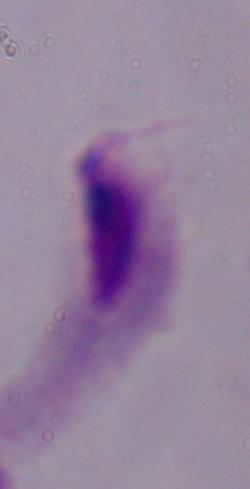
Summary:
  - Magnification: 1000x
  - Modality: photomicrograph
  - Identification: trichomonad